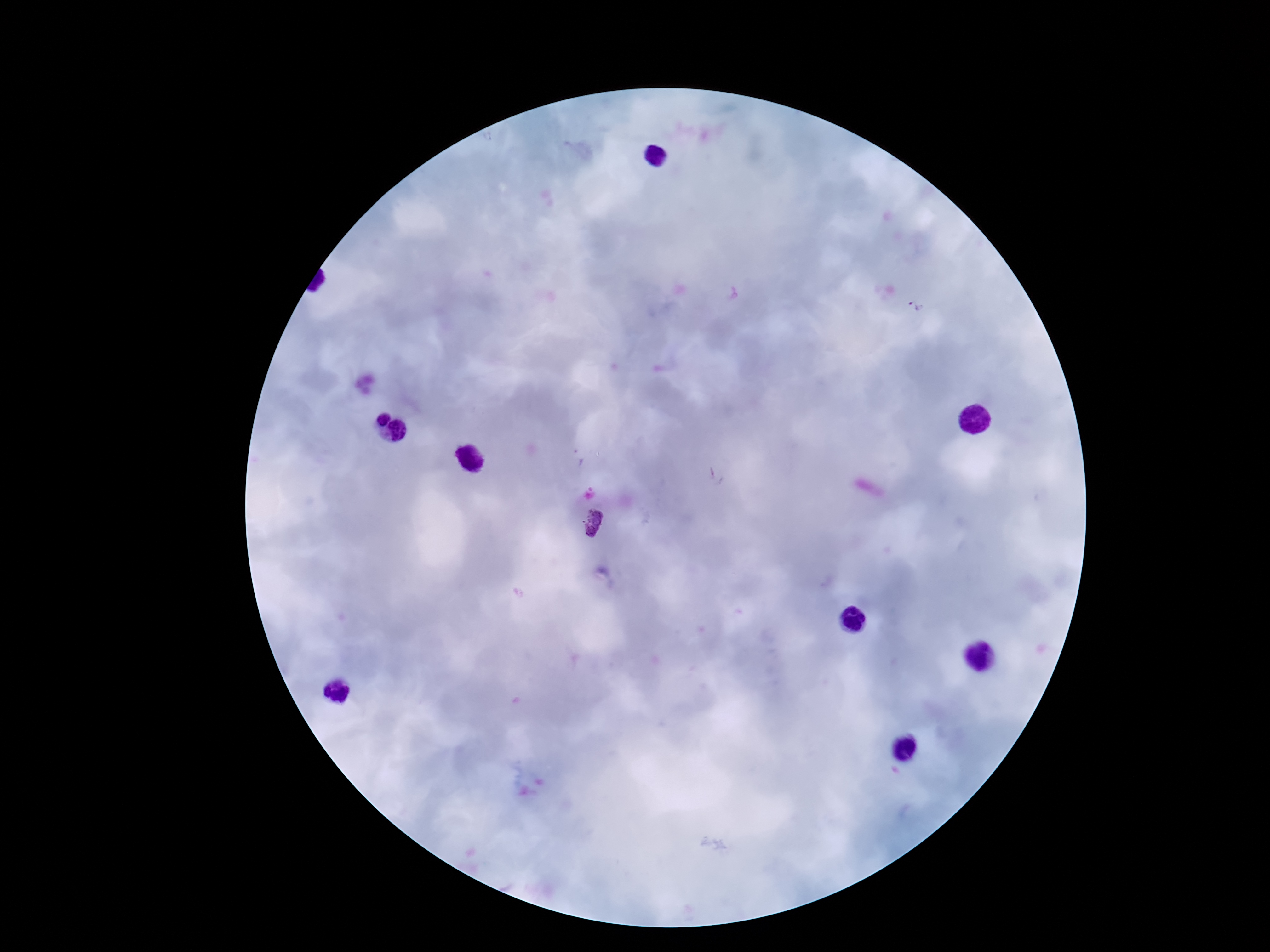
Approximate object centers, in pixels from the top-left corner. Plasmodium parasite locations: (x=913, y=309), (x=593, y=523). Image is 1270×952 pixels. Thick blood film. Giemsa stain. 100x magnification. One field from this slide. Patient malaria status: infected. Photographed through the microscope eyepiece with a smartphone camera.